Assess this cell for malaria.
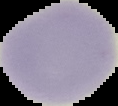
It is uninfected.

{
  "image_size": "118×106 pixels",
  "preparation": "thin blood smear",
  "image_type": "cell region segmented out of the field of view; surrounding area masked to black"
}